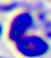
Micrograph. 400x magnification. A white blood cell is seen.